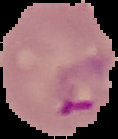

Segmented cell region on a black background. Malaria status: parasitized. From a thin blood film. Image is 118×139 pixels.